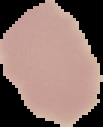
preparation = thin blood film
result = no malaria parasites detected
image size = 103×127 pixels
image type = segmented cell region on a black background